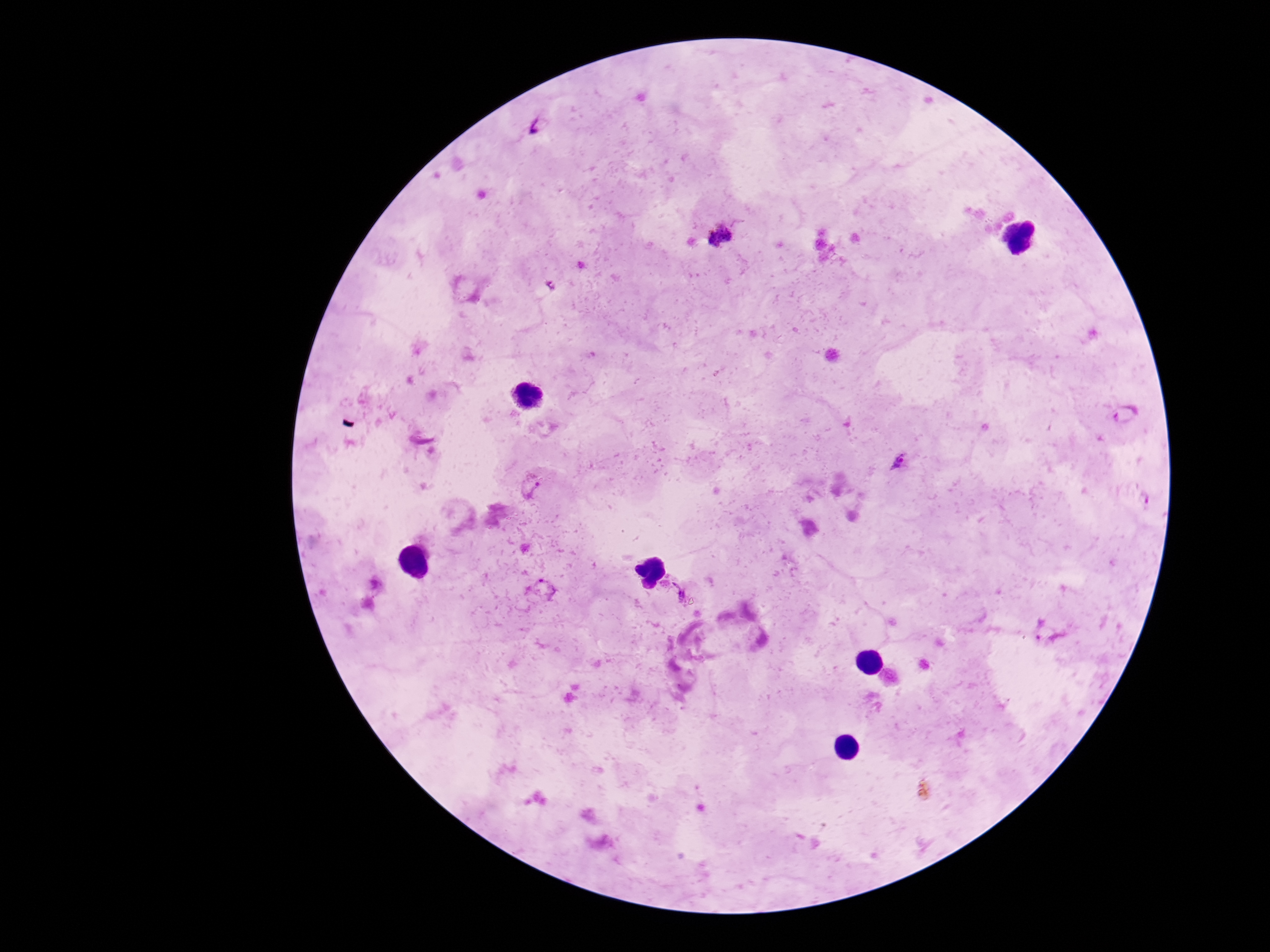
Approximate centers as {x, y} in pixels.
Summary:
  - Plasmodium parasite locations: {538, 125}, {721, 235}, {1126, 413}, {900, 460}, {529, 488}, {1147, 499}, {546, 589}, {678, 590}, {1044, 633}
  - Magnification: 100x
  - Capture: smartphone camera through the microscope eyepiece
  - Stain: Giemsa
  - Image size: 1270×952 pixels
  - Patient malaria status: positive
  - Preparation: thick peripheral-blood smear
  - Field of view: single